Report the malaria status of this cell.
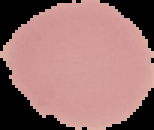

It is uninfected.

preparation: thin blood smear
image_type: segmented cell region with the area outside set to black
image_size: 154×130 pixels